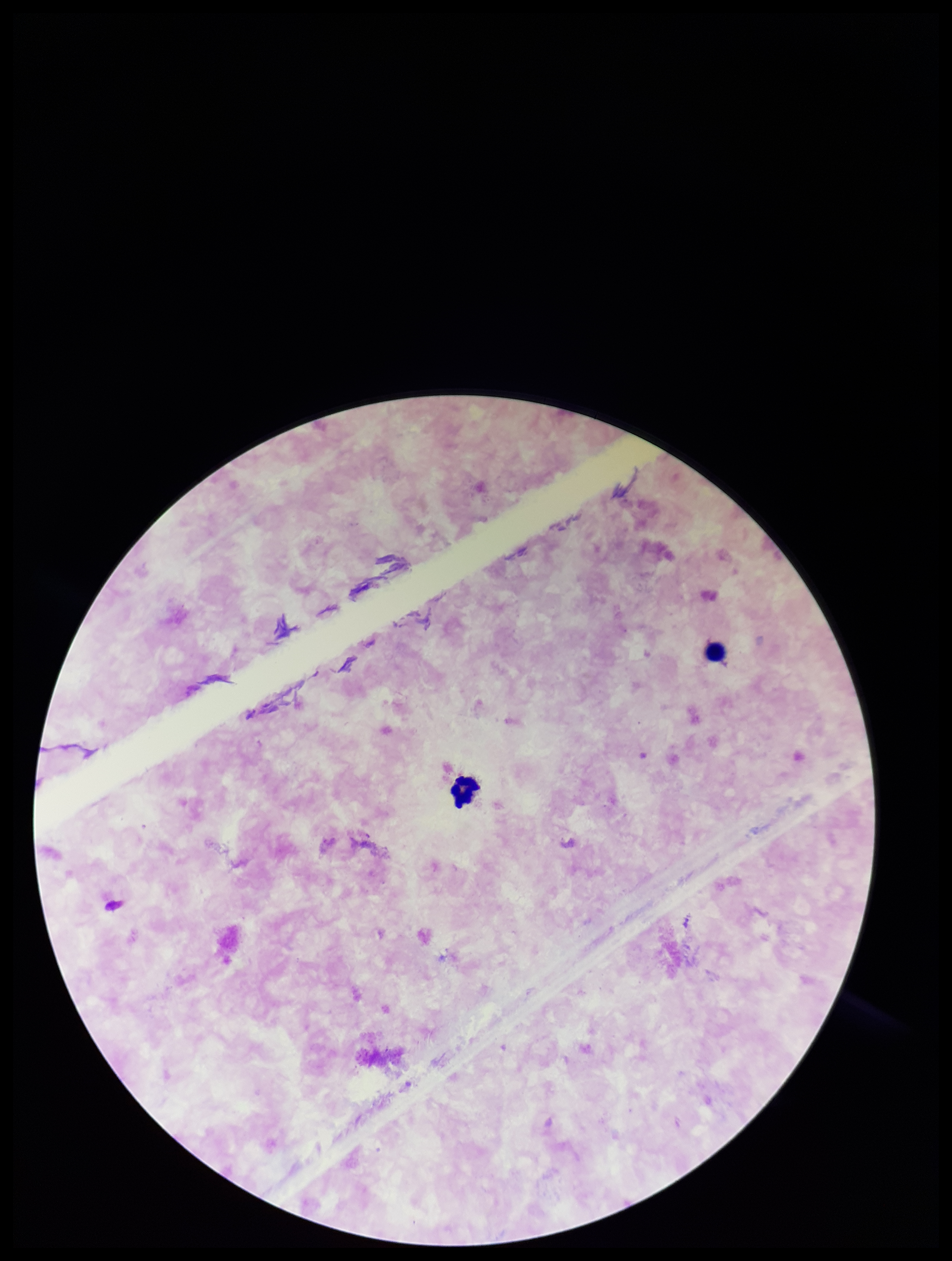

Patient malaria status: negative. Parasite count: 0. Smartphone photograph taken through the eyepiece of a microscope. Image is 952×1261 pixels. Preparation: thick blood smear. Single field of view. Stained with Giemsa. Leukocyte count: 2. Plasmodium parasites: none detected.